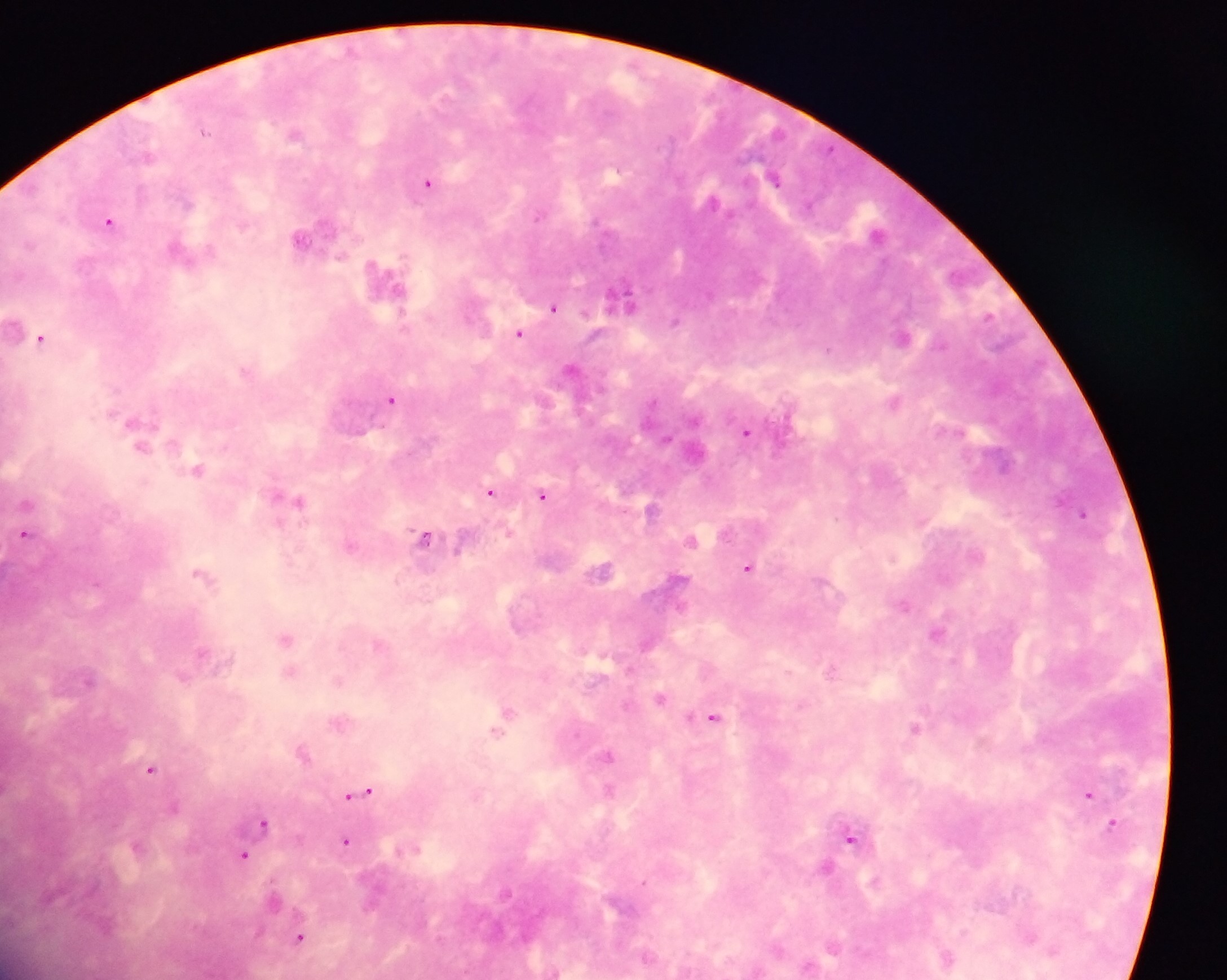
{
  "field_of_view": "single",
  "preparation": "thick blood film",
  "image_size": "1227×980 pixels",
  "country": "Ghana",
  "capture": "mobile-phone photograph through a microscope",
  "malaria_parasite_locations": "approximate centers as x y in pixels: 204 131; 296 133; 775 178; 428 183; 186 201; 712 202; 108 221; 876 232; 301 238; 177 248; 387 281; 619 300; 553 307; 988 314; 675 320; 12 325; 520 333; 41 338; 828 349; 244 370; 392 398; 895 401; 746 431; 137 432; 197 469; 490 491; 543 495; 297 500; 26 503; 652 509; 1083 512; 26 517; 25 533; 425 536; 691 539; 350 545; 976 553; 748 566; 603 569; 200 572; 903 603; 937 632; 286 637; 647 642; 377 644; 830 670; 289 672; 660 697; 506 713; 713 716; 915 726; 302 751; 607 754; 151 768; 609 789; 360 792; 1088 793; 263 822; 1112 823; 256 834; 850 836; 347 841; 244 855; 826 866; 1029 936; 300 937; 947 958"
}